Report the malaria status of this cell.
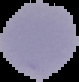

It is parasitized.

image type = segmented cell region on a black background
image size = 79×82 pixels
preparation = thin blood smear